Locate every leukocyte (white blood cell).
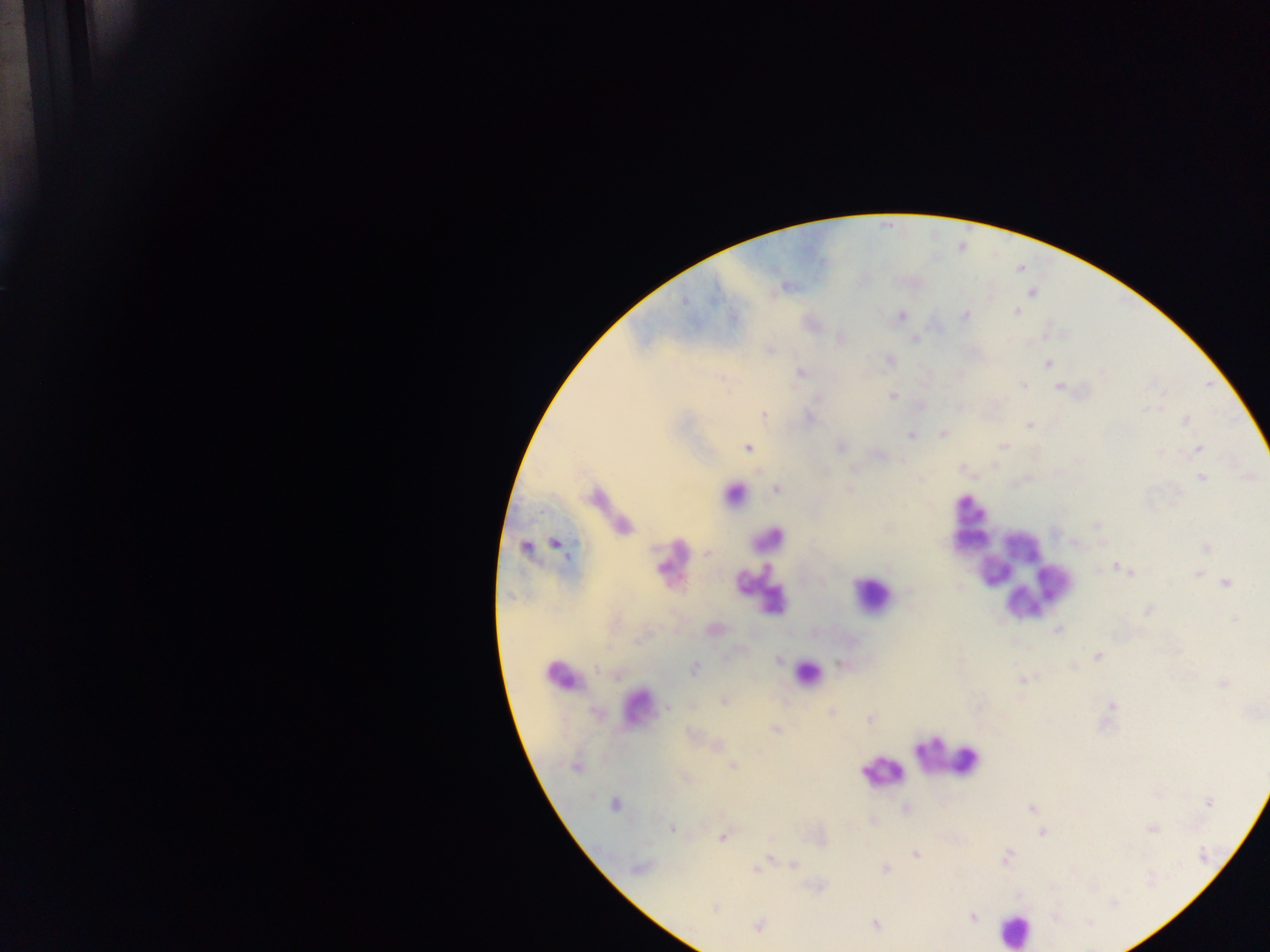
Approximate centers as [x, y] in pixels.
Leukocytes: [734, 494], [969, 507], [765, 538], [971, 542], [1021, 546], [669, 559], [994, 572], [1059, 583], [757, 591], [871, 594], [1023, 603], [806, 672], [562, 674], [637, 702], [948, 758], [880, 773], [1015, 930].

image_size: 1270×952 pixels
preparation: thick blood film
plasmodium_parasite_locations: 'approximate centers as [x, y] in pixels: [1033, 292], [685, 301], [1016, 311], [901, 316], [966, 316], [914, 340], [769, 350], [890, 359], [1048, 364], [801, 372], [1023, 384], [1059, 387], [893, 396], [818, 398], [763, 414], [811, 418], [1186, 420], [1029, 425], [943, 433], [910, 435], [1004, 445], [842, 447], [748, 448], [1199, 448], [826, 471], [1202, 477], [849, 489], [776, 490], [1097, 526], [555, 543], [525, 547], [1207, 548], [707, 553], [1116, 567], [1130, 573], [1197, 573], [1226, 582], [908, 592], [1148, 610], [1235, 619], [1058, 629], [1098, 656], [780, 660], [1073, 666], [694, 668], [596, 669], [1023, 680], [1223, 684], [725, 701], [1112, 705], [667, 707], [596, 713], [830, 713], [869, 719], [776, 730], [718, 745], [733, 766], [575, 767], [685, 778], [1209, 803], [615, 804], [1030, 809], [671, 828], [1151, 828], [1042, 833], [723, 837], [917, 855], [1006, 857], [771, 858], [793, 864], [639, 866], [762, 866], [757, 869], [885, 869], [715, 908], [973, 917], [1089, 923], [758, 925], [875, 925]'
country: Ghana
capture: mobile-phone photograph through a microscope
field_of_view: single